Comment on the morphology of the red blood cells.
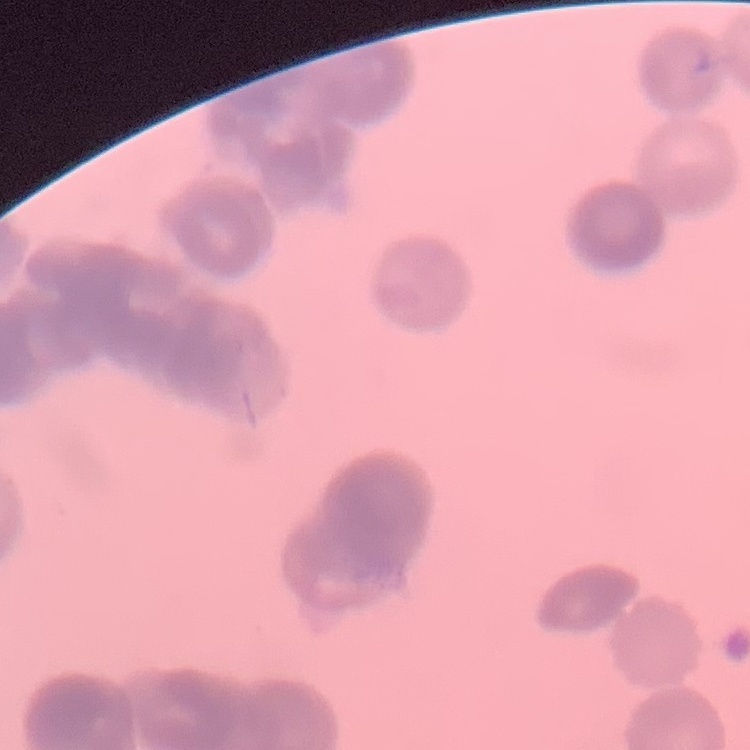
Rouleaux formation.

Summary:
  - Stain: Field's or Giemsa
  - Preparation: thin blood film
  - Image type: square crop of a larger photomicrograph